Report the malaria status of this cell.
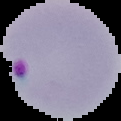
Parasitized.

image size = 121×121 pixels
preparation = thin blood film
image type = cell region segmented out of the field of view; surrounding area masked to black